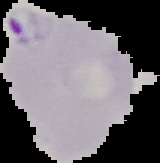

{
  "image_type": "segmented cell region on a black background",
  "preparation": "thin blood smear",
  "image_size": "160×163 pixels",
  "malaria_status": "parasitized"
}